Classify this cell by malaria status.
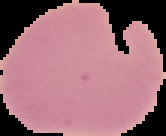

It is uninfected.

Summary:
  - Preparation: thin blood film
  - Image size: 166×136 pixels
  - Image type: segmented cell region on a black background